Locate every leukocyte (white blood cell).
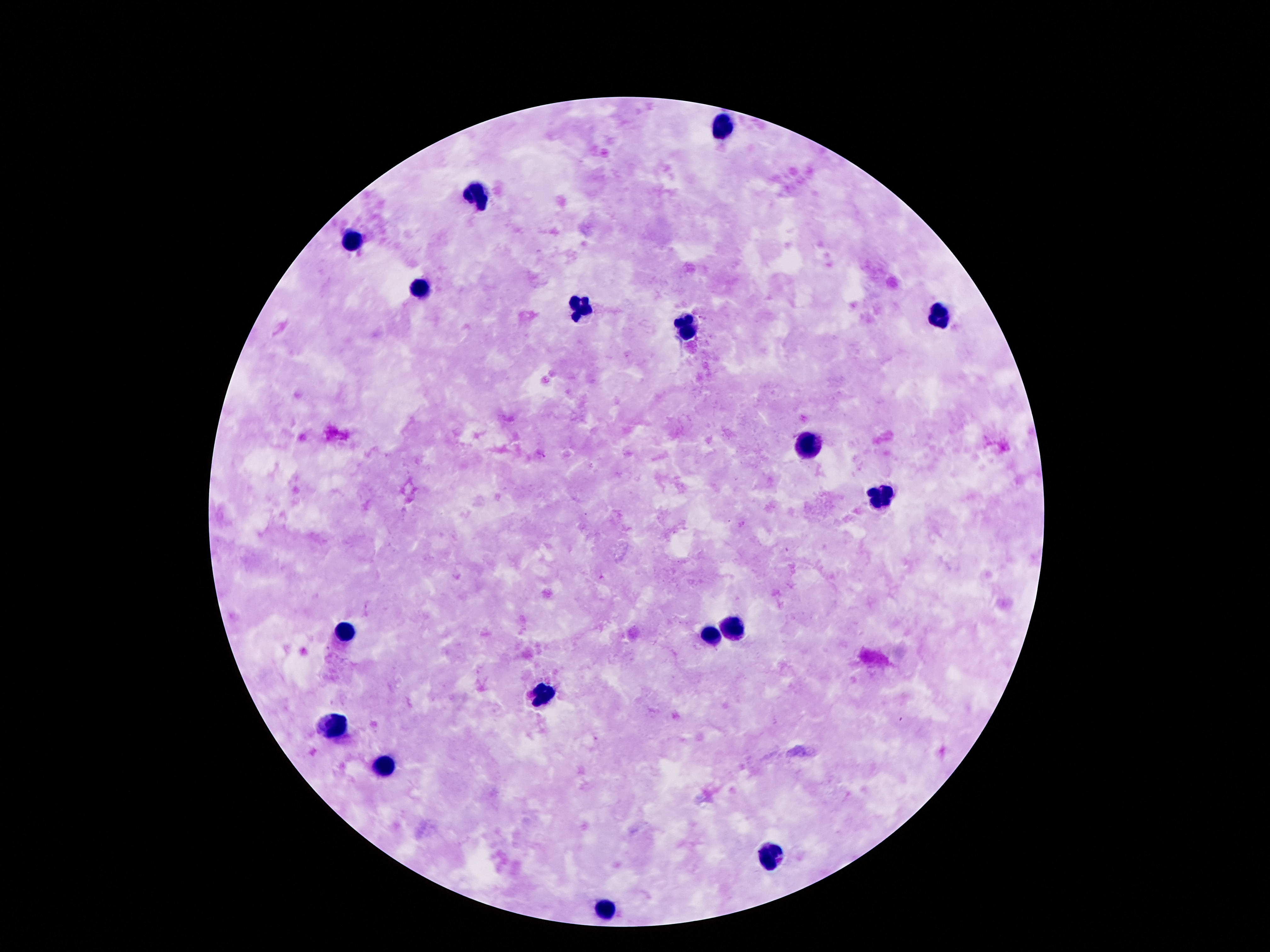
Approximate centers as (x, y) in pixels.
Leukocytes: (718, 126), (476, 195), (353, 241), (418, 290), (581, 305), (936, 315), (688, 328), (808, 442), (881, 498), (730, 626), (342, 633), (711, 634), (541, 696), (336, 726), (382, 767), (772, 853), (607, 913).

patient malaria status = uninfected
field of view = single
magnification = 100x
capture = smartphone camera through the microscope eyepiece
preparation = thick blood film
image size = 1270×952 pixels
stain = Giemsa